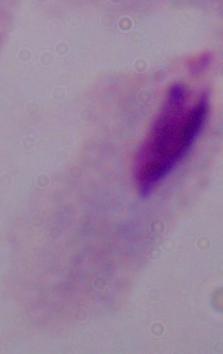
{
  "identification": "trichomonad",
  "modality": "micrograph",
  "magnification": "1000x"
}